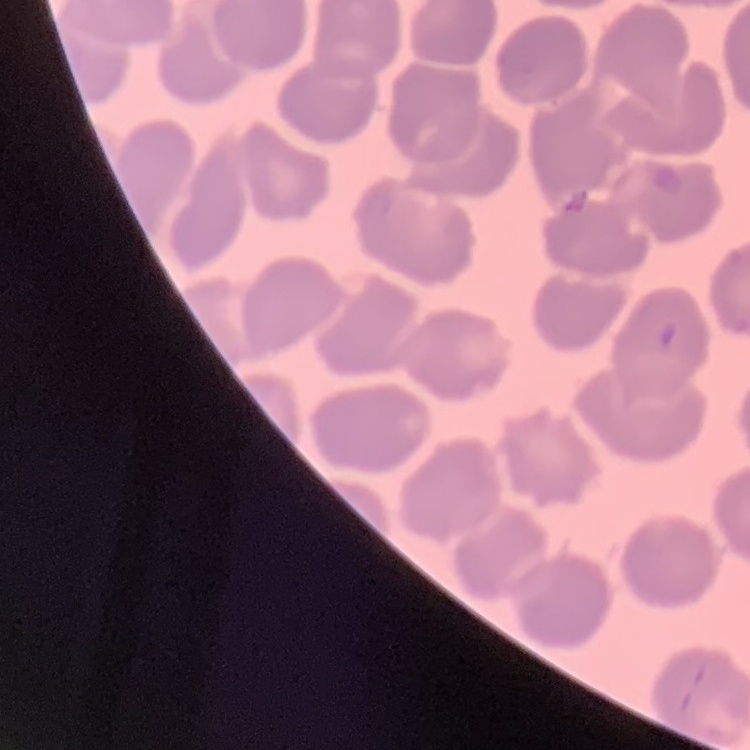

The erythrocytes exhibit no rouleaux formation. Square crop of a larger photomicrograph. Thin blood film. Field's or Giemsa stain.